Assess this cell for malaria.
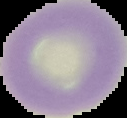
Uninfected.

preparation = thin blood smear
image size = 127×118 pixels
image type = segmented cell region with the area outside set to black